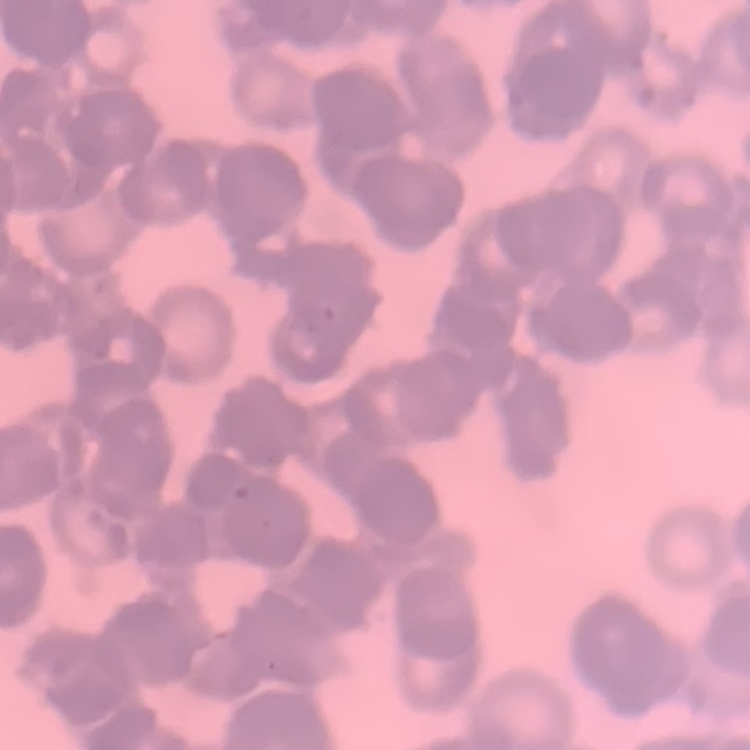 The erythrocytes exhibit rouleaux formation. Field's or Giemsa stain. One tile cut from a larger photomicrograph. Thin peripheral smear.